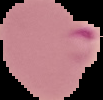
Summary:
  - Preparation: thin blood film
  - Image size: 103×100 pixels
  - Result: malaria parasites detected
  - Image type: segmented cell region with the area outside set to black